Assess the morphology of the red blood cells.
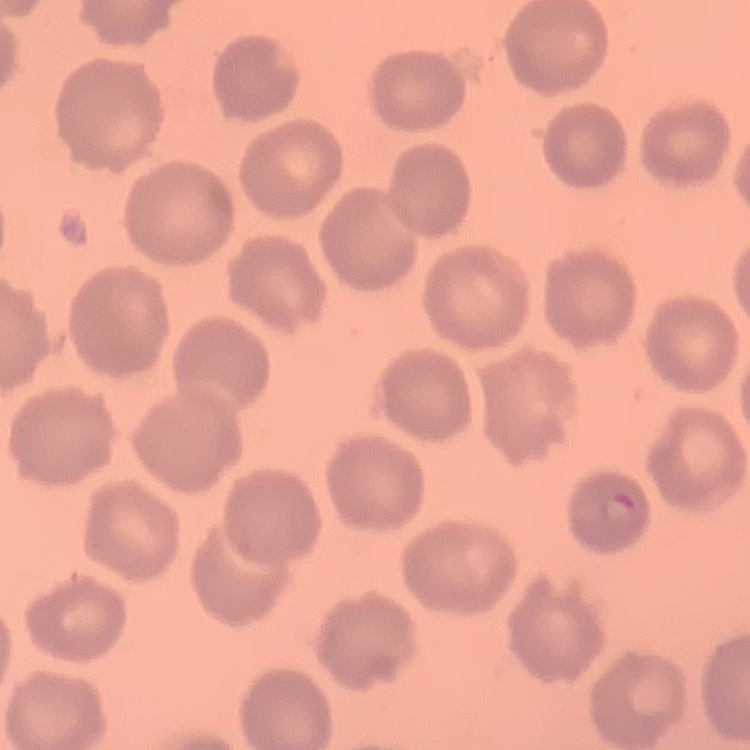

No rouleaux formation.

Summary:
  - Stain: Field's or Giemsa
  - Preparation: thin blood smear
  - Image type: square crop of a larger photomicrograph